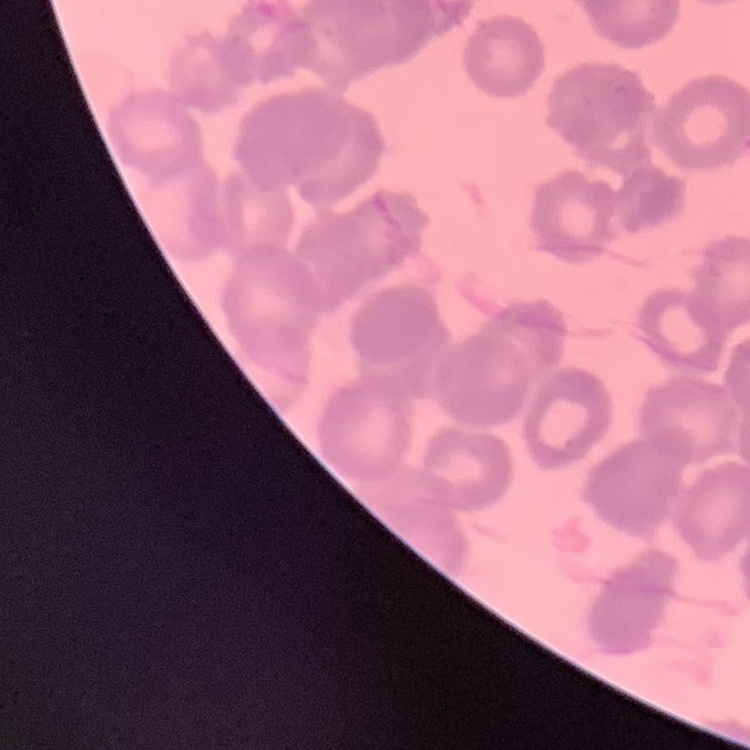

The red blood cells exhibit rouleaux formation. One tile cut from a larger photomicrograph. Thin blood smear. Stained with either Field's or Giemsa.